Identify the preparation type.
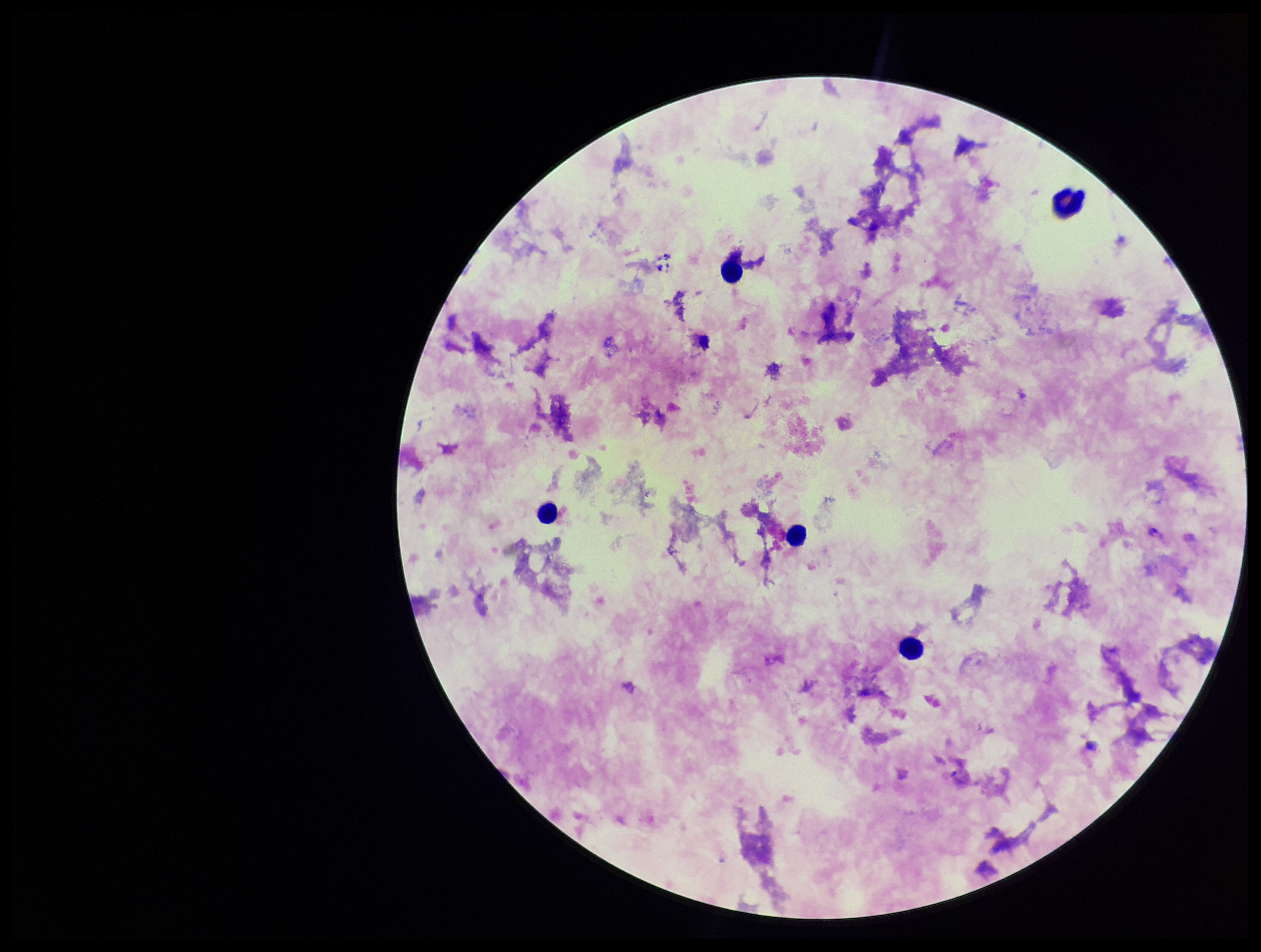
It is a thick blood smear.

Summary:
  - Capture: smartphone photograph through the microscope eyepiece
  - Leukocyte count: 5
  - Field of view: single
  - Patient malaria status: positive
  - Plasmodium parasites: seen
  - Species reported for this patient: Plasmodium falciparum
  - Stain: Giemsa
  - Parasite count: 1
  - Image size: 1261×952 pixels